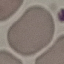
Result: no malaria parasites detected. Cell patch, automatically extracted from a larger field of view and resized to 64 × 64 pixels. Thin blood film. Acquired by smartphone through the microscope eyepiece. Giemsa stain.